Classify this cell by malaria status.
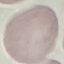

It is uninfected.

Summary:
  - Preparation: thin blood film
  - Stain: Giemsa
  - Capture: smartphone camera at the microscope eyepiece
  - Image type: automatically extracted cell patch, resized to 64 × 64 pixels